Locate and identify every blood parasite.
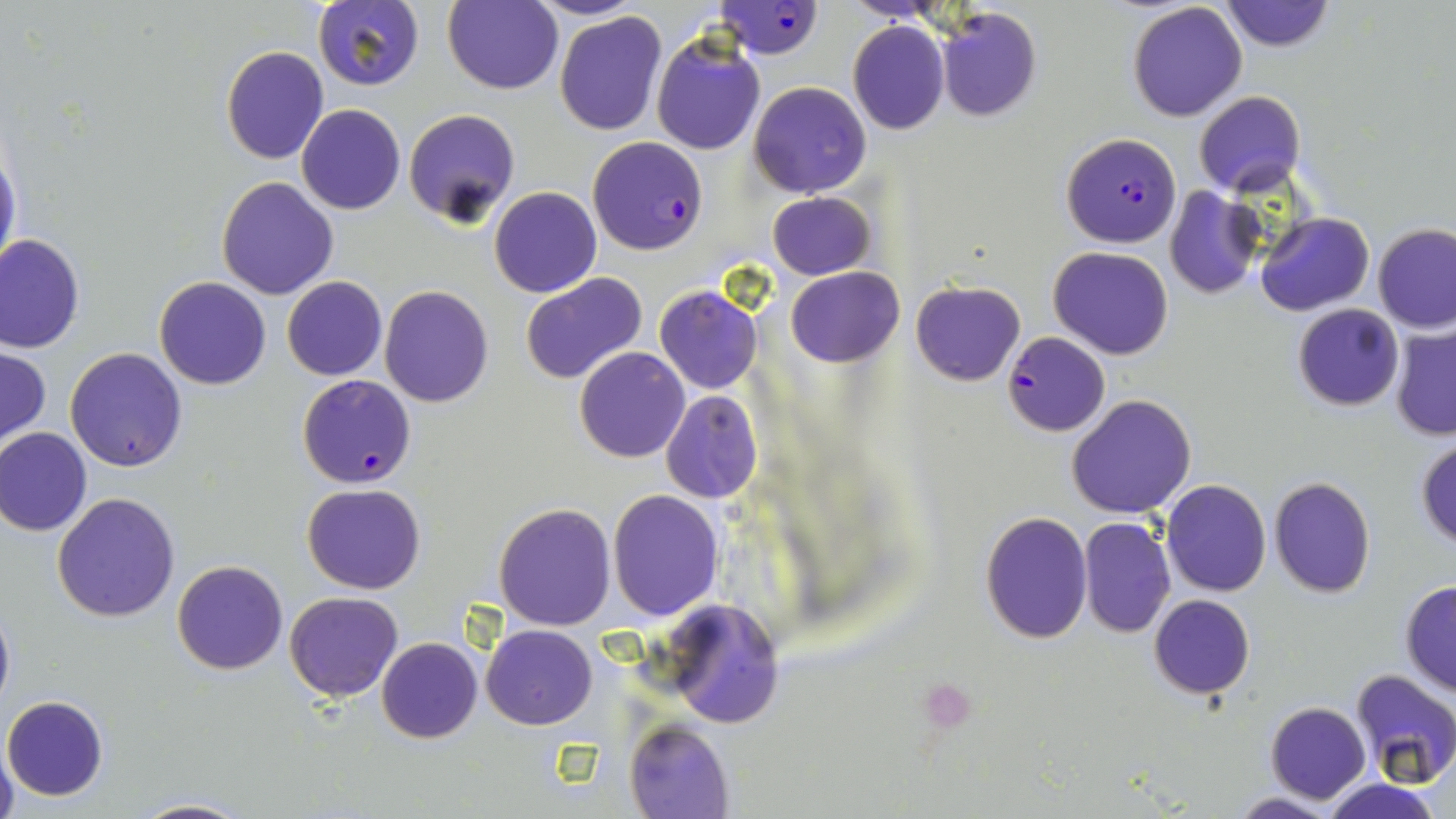

Approximate bounding boxes as (x1,y1)-(x2,y2) corner pairs in pixels.
Plasmodium falciparum-infected red blood cells: (712,1)-(826,58), (1061,131)-(1182,247), (587,136)-(708,255), (1004,332)-(1110,437), (297,374)-(418,490).
No Plasmodium ovale, Plasmodium malariae, Plasmodium vivax, Babesia divergens, or Trypanosoma brucei observed.

Summary:
  - Uninfected red blood cell locations: (314,1)-(427,91), (443,1)-(563,95), (1219,1)-(1336,52), (1127,3)-(1248,122), (936,7)-(1041,122), (554,11)-(666,136), (847,21)-(949,135), (650,32)-(766,155), (221,46)-(330,164), (748,81)-(872,198), (1193,90)-(1304,197), (297,104)-(405,214), (403,108)-(519,226), (0,143)-(20,280), (216,176)-(339,299), (489,186)-(601,297), (1165,187)-(1262,298), (767,191)-(877,280), (1256,212)-(1375,316), (1373,223)-(1456,334), (0,235)-(85,353), (1049,246)-(1173,358), (786,267)-(904,366), (521,273)-(648,386), (154,276)-(270,390), (282,277)-(388,380), (910,280)-(1026,386), (380,285)-(492,406), (654,285)-(763,394), (1292,303)-(1404,411), (1389,323)-(1456,441), (0,344)-(50,449), (65,347)-(187,472), (574,347)-(689,463), (660,389)-(762,502), (1066,394)-(1197,518), (0,428)-(91,537), (1415,437)-(1456,550), (1268,476)-(1376,598), (1160,479)-(1272,597), (301,483)-(425,595), (607,490)-(725,621), (51,493)-(181,623), (493,503)-(617,631), (978,511)-(1093,644), (1078,516)-(1175,637), (172,559)-(287,675), (1400,582)-(1456,696), (285,591)-(402,702), (1148,594)-(1255,699), (0,596)-(15,718), (656,599)-(785,729), (482,625)-(598,729), (376,637)-(482,743), (1349,667)-(1456,786), (2,697)-(109,801), (1265,701)-(1370,803), (625,719)-(733,817), (1,739)-(18,819), (1318,777)-(1445,819), (1230,792)-(1342,818), (131,797)-(252,818)
  - Platelet locations: (917,676)-(978,730)
  - Slide-level diagnosis: Plasmodium falciparum
  - Magnification: 1000x
  - Field of view: one of a larger specimen
  - Preparation: thin blood smear
  - Image size: 1456×819 pixels
  - Modality: optical microscopy
  - Stain: May-Grünwald-Giemsa